Give the position of every leukocyte visible.
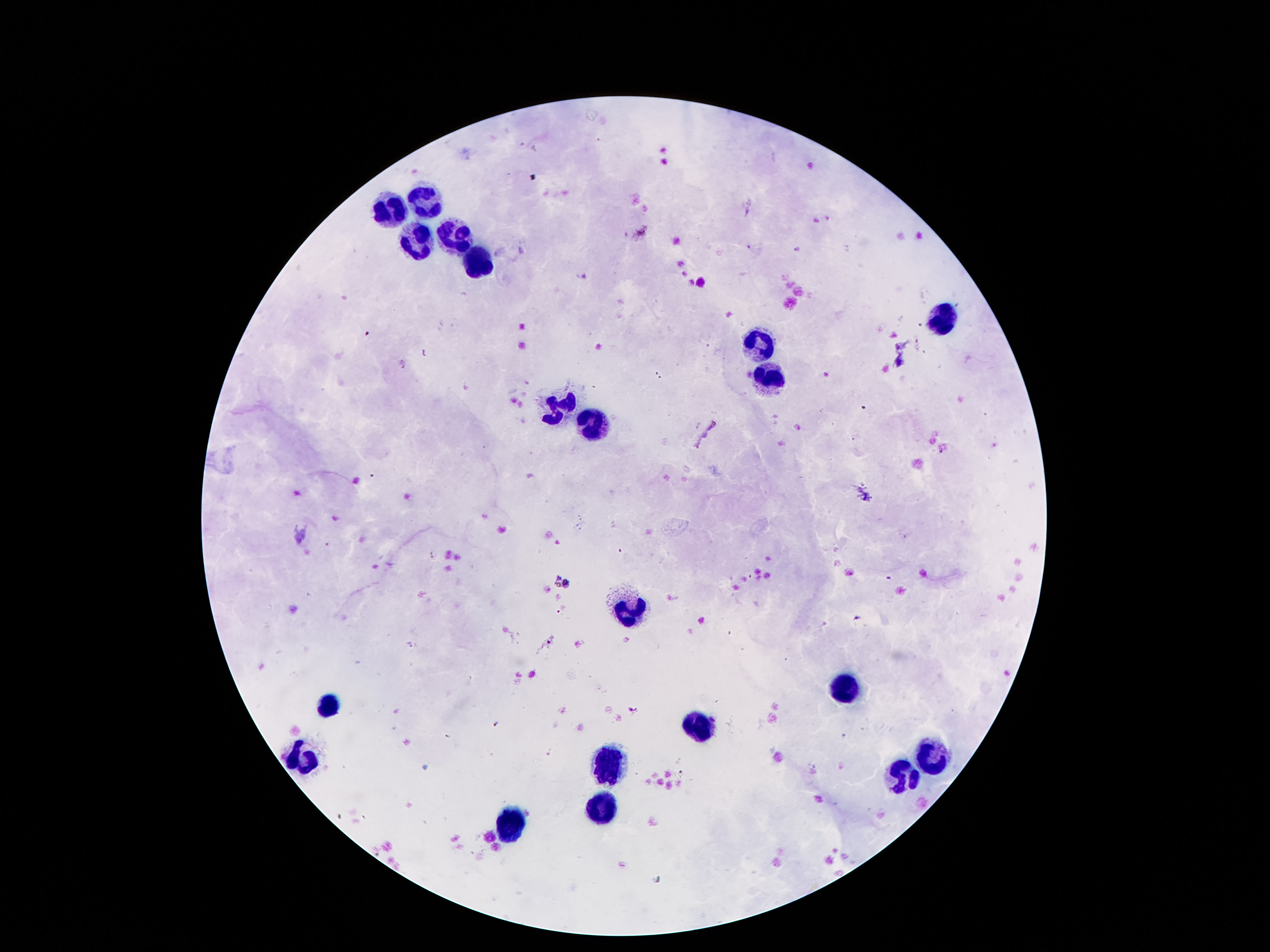
Approximate centers as {x, y} in pixels.
Leukocytes: {424, 201}, {387, 211}, {449, 234}, {413, 239}, {474, 258}, {942, 317}, {759, 347}, {765, 376}, {557, 405}, {586, 427}, {628, 611}, {841, 691}, {328, 706}, {697, 727}, {930, 755}, {300, 758}, {605, 763}, {902, 780}, {605, 810}, {508, 825}.

Summary:
  - Patient malaria status: uninfected
  - Image size: 1270×952 pixels
  - Field of view: one from this slide
  - Capture: smartphone camera through the microscope eyepiece
  - Stain: Giemsa
  - Preparation: thick blood smear
  - Magnification: 100x